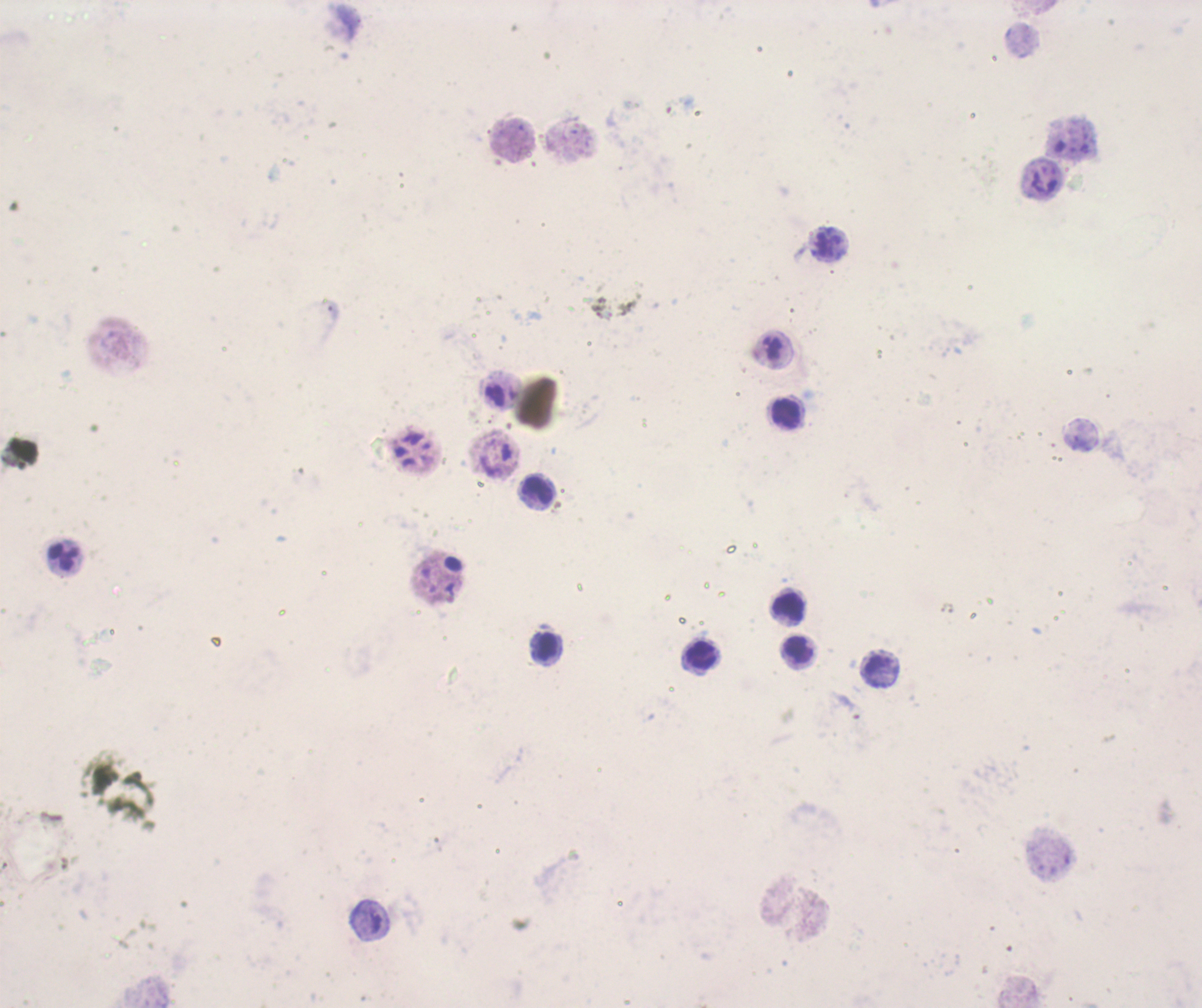

Approximate object centers, in pixels from the top-left corner.
Summary:
  - Leukocyte locations: (x=787, y=415), (x=537, y=490), (x=789, y=608), (x=545, y=647), (x=797, y=649), (x=700, y=655)
  - Result: no malaria parasites detected
  - Preparation: thick blood smear
  - Magnification: 100x
  - Image size: 1202×1008 pixels
  - Field of view: one from this slide
  - Stain: Romanowsky
  - Background quality: unsatisfactory
  - Context: previously used in an actual diagnosis
  - Coloration quality: bad